Describe the morphology of the erythrocytes.
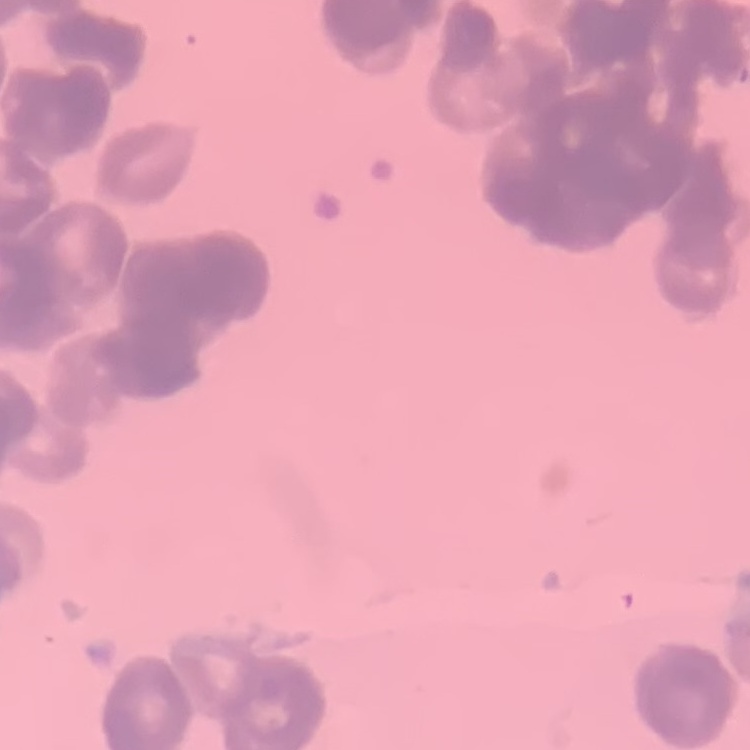
Rouleaux formation.

Summary:
  - Stain: Field's or Giemsa
  - Image type: one tile cut from a larger photomicrograph
  - Preparation: thin blood film